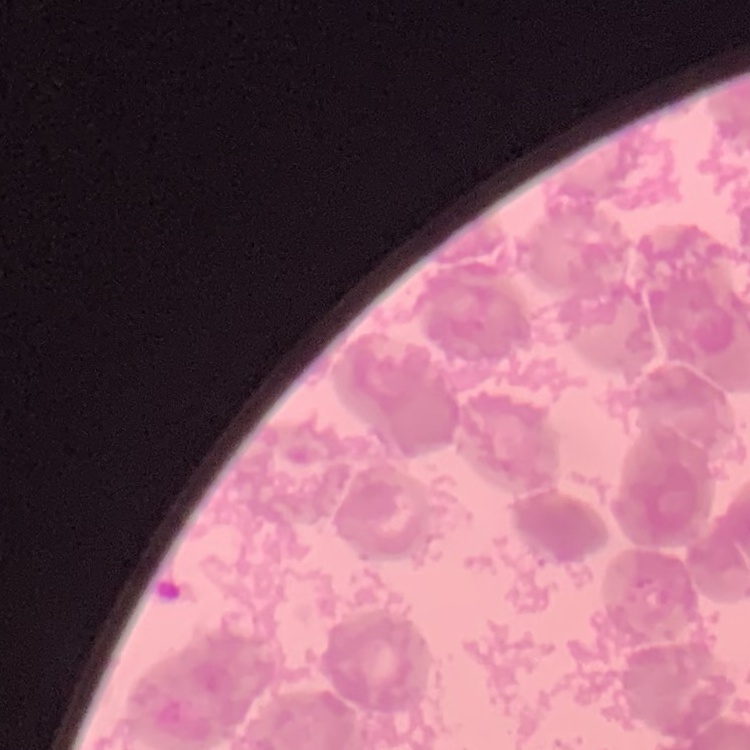 The red blood cells show rouleaux formation. Thin blood smear. Stained with either Field's or Giemsa. One tile cut from a larger photomicrograph.